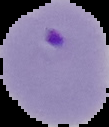

Summary:
  - Result: Plasmodium parasites detected
  - Image type: cell region segmented out of the field of view; surrounding area masked to black
  - Image size: 109×127 pixels
  - Preparation: thin blood film